State which parasite is depicted.
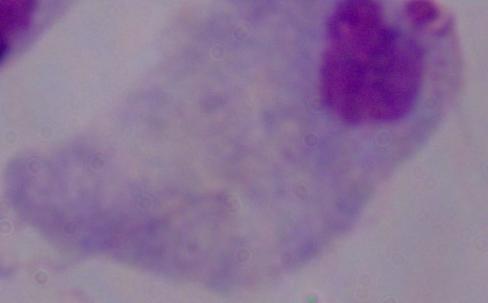
This is a trichomonad.

magnification: 1000x
modality: micrograph